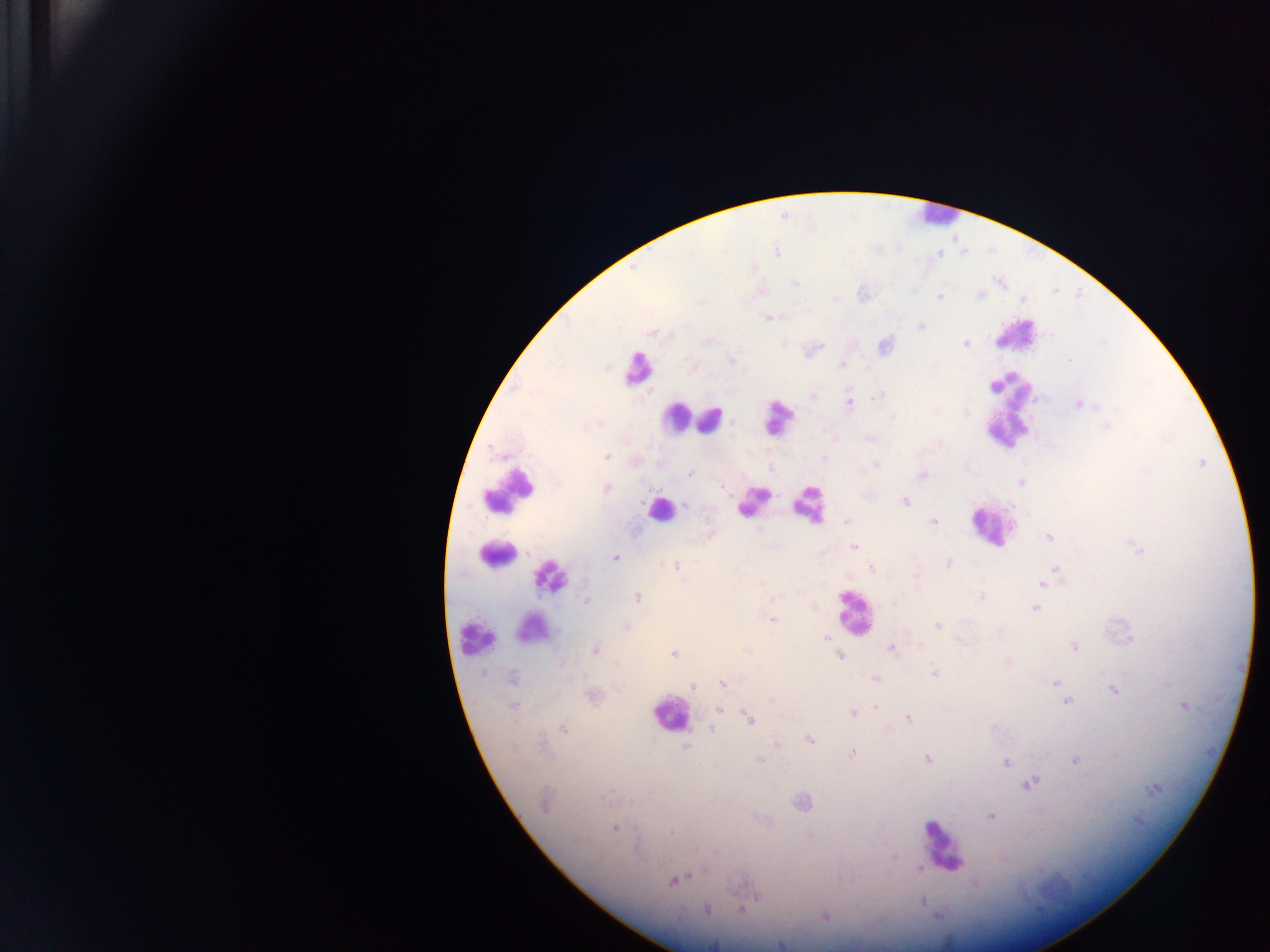

Approximate centers as [x, y] in pixels.
Summary:
  - Leukocyte locations (subset; some below the resolvable size): [933, 216], [1016, 334], [639, 366], [1006, 411], [676, 417], [777, 417], [710, 420], [509, 488], [751, 502], [808, 503], [660, 509], [990, 526], [495, 554], [552, 578], [854, 613], [533, 632], [476, 635], [669, 714], [942, 845]
  - Plasmodium parasite locations: [776, 252], [940, 254], [795, 283], [979, 294], [939, 297], [767, 317], [921, 326], [653, 333], [672, 334], [966, 344], [885, 345], [732, 359], [1070, 359], [690, 366], [842, 366], [812, 396], [877, 396], [849, 403], [1079, 404], [966, 411], [893, 417], [1107, 427], [871, 438], [605, 457], [824, 458], [876, 465], [690, 474], [922, 474], [1021, 482], [723, 486], [607, 488], [905, 501], [685, 505], [847, 521], [934, 522], [1048, 537], [853, 547], [1137, 549], [615, 557], [949, 563], [677, 565], [870, 568], [1056, 569], [916, 580], [1043, 583], [638, 597], [982, 597], [587, 601], [894, 603], [1035, 608], [773, 620], [626, 625], [937, 626], [827, 636], [1074, 647], [890, 649], [595, 650], [674, 654], [841, 657], [934, 674], [512, 677], [875, 679], [1055, 682], [723, 683], [1167, 684], [693, 687], [1114, 690], [594, 695], [772, 699], [1068, 702], [513, 705], [875, 707], [1184, 707], [719, 709], [853, 713], [908, 718], [749, 719], [563, 730], [712, 730], [810, 739], [685, 748], [853, 753], [927, 759], [760, 760], [1075, 761], [1005, 762], [1031, 783], [1153, 789], [545, 803], [801, 803], [990, 816], [614, 828], [810, 835], [920, 869], [673, 881], [706, 909], [742, 910], [825, 917], [780, 944]
  - Image size: 1270×952 pixels
  - Country: Ghana
  - Preparation: thick blood smear
  - Field of view: single
  - Capture: mobile-phone photograph through a microscope